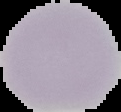

The area outside the segmented cell region is set to black. Image is 121×112 pixels. From a thin blood smear. Result: no malaria parasites seen.